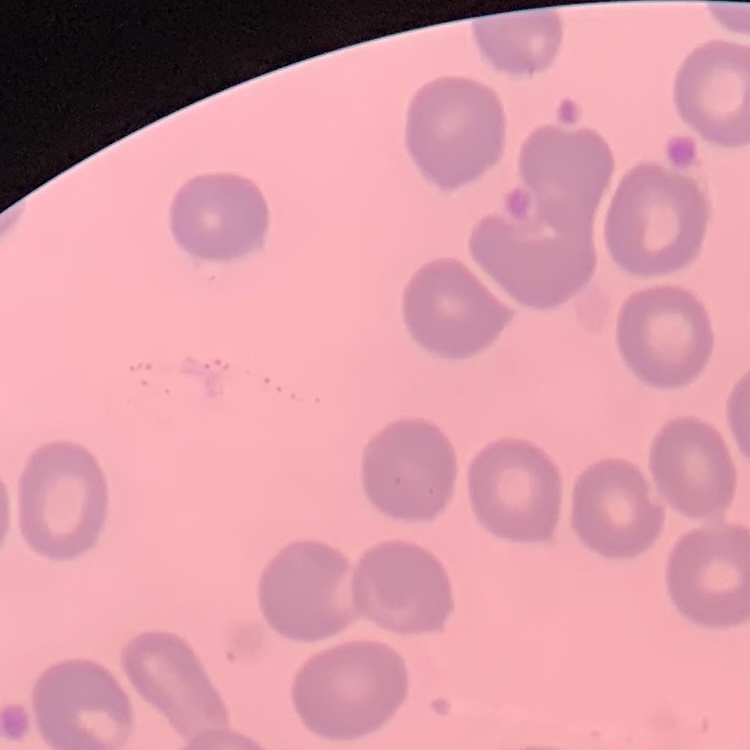
The red blood cells show no rouleaux formation. Field's or Giemsa stain. Thin peripheral smear. One tile cut from a larger photomicrograph.